Identify the parasite.
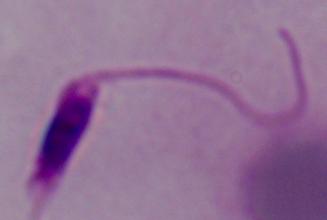

Leishmania.

modality = photomicrograph
magnification = 1000x